Name the cell type shown.
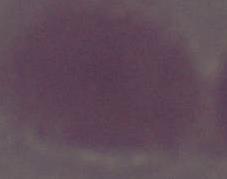
An erythrocyte.

1000x magnification. Photomicrograph.